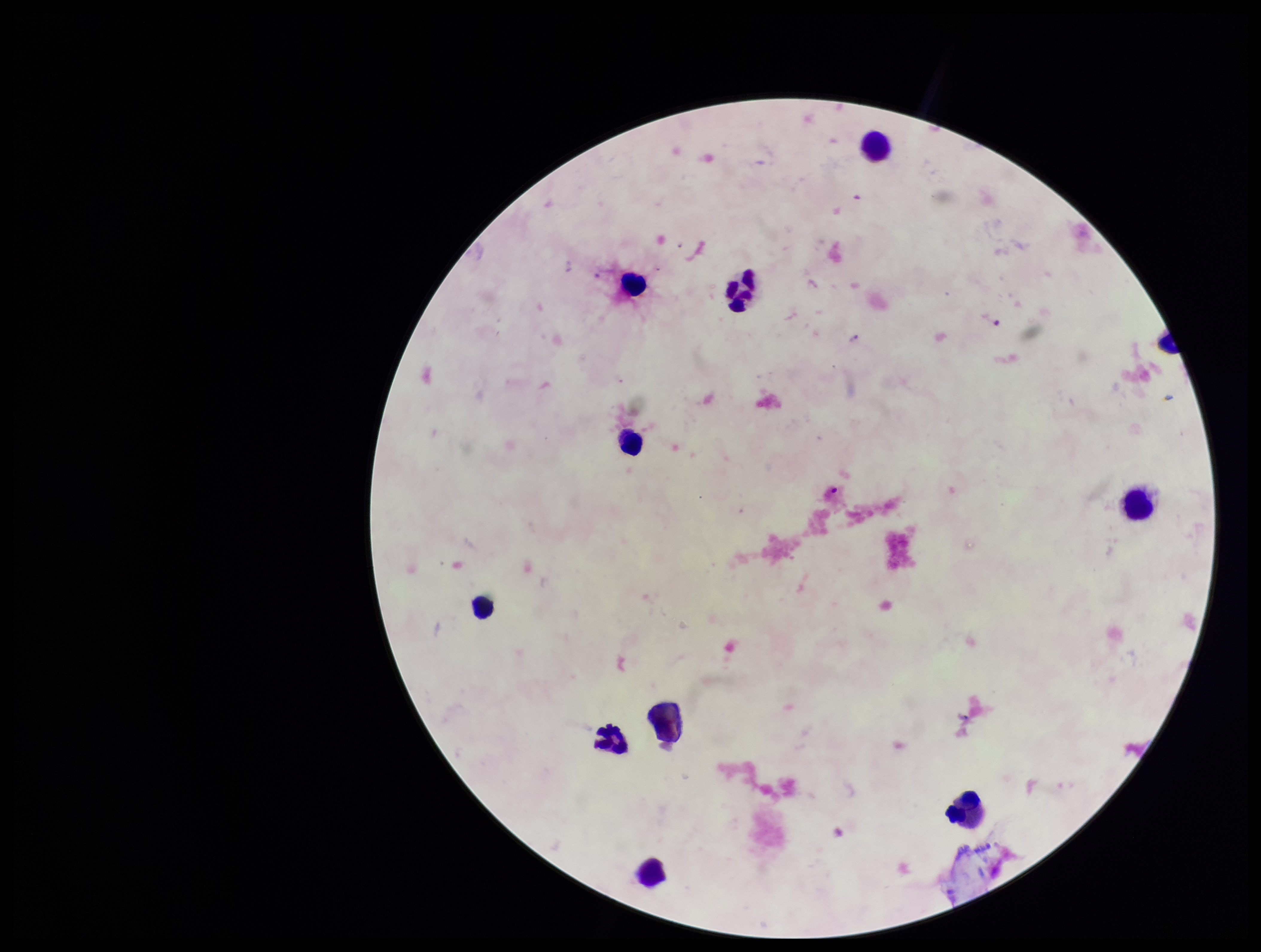
Summary:
  - Leukocyte count: 10
  - Capture: smartphone photograph through the microscope eyepiece
  - Stain: Giemsa
  - Plasmodium parasites: none identified
  - Patient malaria status: negative
  - Parasite count: 0
  - Field of view: one from this slide
  - Image size: 1261×952 pixels
  - Preparation: thick blood smear